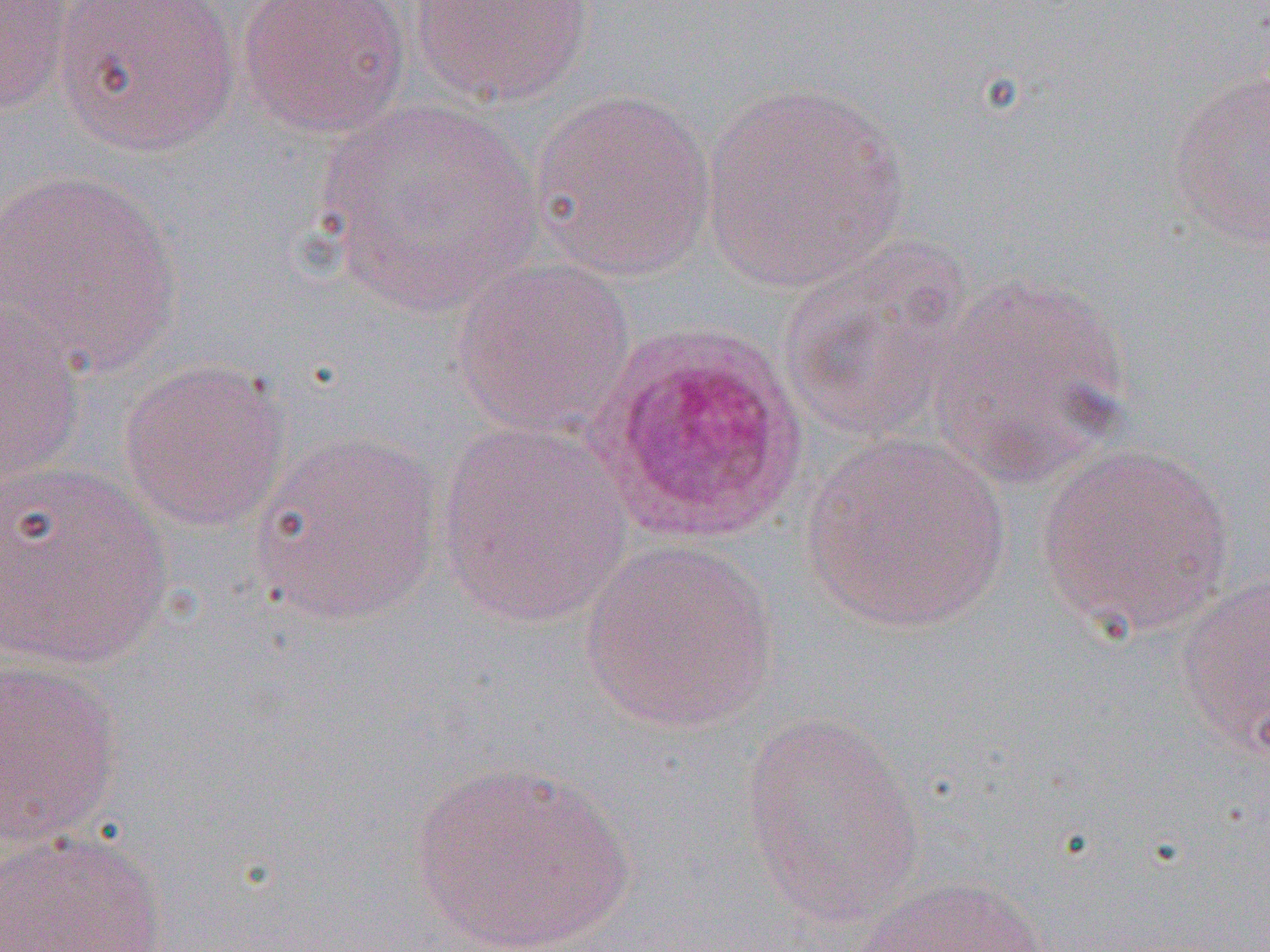
Approximate bounding boxes as (x1,y1)-(x2,y2) corner pairs in pixels. Plasmodium ovale-infected red blood cell locations: (588,319)-(812,549). Uninfected red blood cell locations: (238,0)-(412,139), (407,0)-(596,107), (0,1)-(75,115), (52,1)-(243,156), (1167,71)-(1270,250), (701,80)-(908,292), (529,88)-(716,281), (316,97)-(543,314), (1,169)-(185,375), (778,241)-(973,444), (450,257)-(637,439), (924,272)-(1133,486), (1,304)-(88,489), (118,359)-(293,533), (435,422)-(634,627), (248,430)-(443,627), (800,433)-(1011,635), (1035,441)-(1235,638), (0,460)-(174,671), (582,537)-(778,733), (1174,574)-(1270,755), (0,656)-(125,850), (737,712)-(927,926), (408,759)-(637,952), (0,830)-(168,951), (854,874)-(1054,951). Slide-level diagnosis: Plasmodium ovale. One field of a larger specimen. 1000x magnification. Image is 1270×952 pixels. Light microscopy. Thin blood smear.